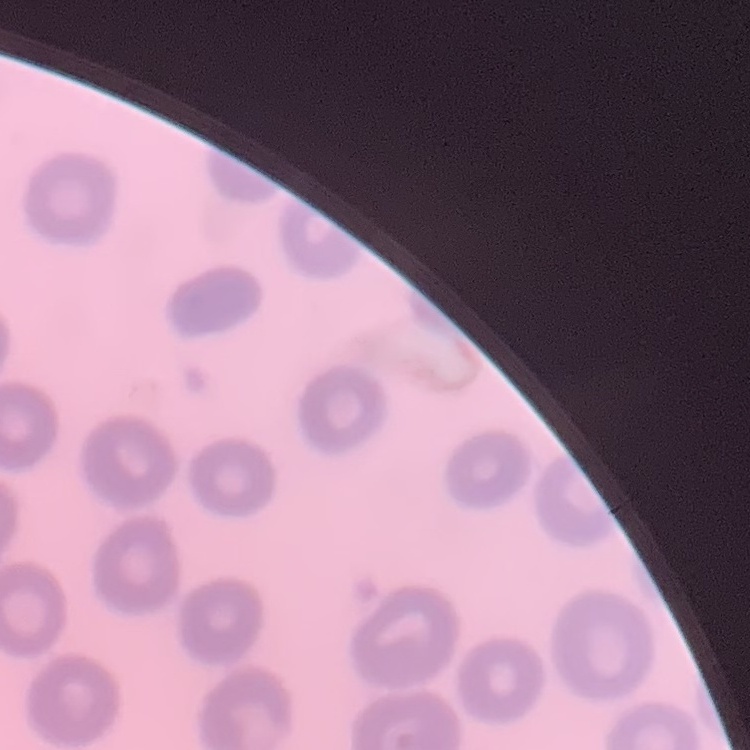
Summary:
  - Erythrocyte morphology: no rouleaux formation
  - Preparation: thin blood smear
  - Stain: Field's or Giemsa
  - Image type: square crop of a larger photomicrograph